State the preparation type.
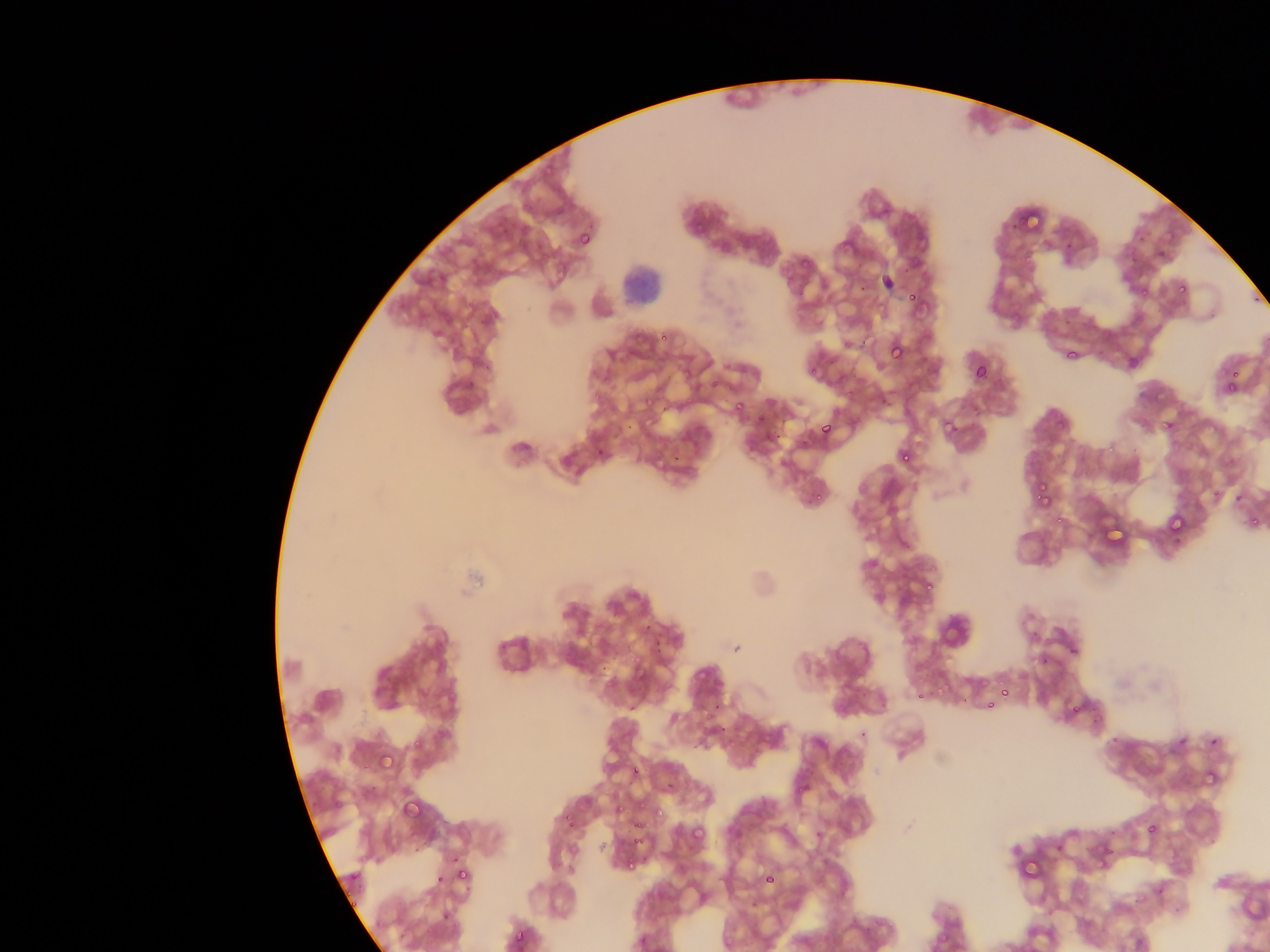
This is a thin smear.

plasmodium_parasite_locations: 'approximate bounding boxes as (left, top, right, bottom) in pixels: (1025, 211, 1044, 231), (689, 221, 705, 235), (578, 231, 593, 247), (798, 259, 809, 269), (1177, 284, 1187, 295), (1136, 288, 1149, 303), (907, 290, 921, 305), (660, 332, 670, 342), (887, 340, 904, 360), (1065, 349, 1077, 359), (808, 354, 820, 374), (972, 364, 987, 380), (1228, 369, 1239, 380), (1223, 374, 1238, 392), (844, 381, 857, 399), (583, 388, 606, 403), (637, 396, 654, 413), (734, 401, 746, 414), (756, 415, 766, 425), (1163, 419, 1175, 432), (941, 421, 955, 432), (820, 422, 834, 435), (1103, 444, 1117, 457), (898, 449, 913, 463), (671, 453, 680, 461), (1034, 480, 1048, 496), (1207, 489, 1220, 503), (807, 490, 824, 503), (1039, 494, 1053, 508), (1169, 514, 1187, 534), (1055, 515, 1065, 525), (1249, 515, 1260, 532), (1105, 518, 1125, 543), (922, 578, 937, 593), (639, 618, 654, 633), (652, 639, 668, 653), (1069, 646, 1079, 656), (936, 680, 949, 700), (1001, 690, 1010, 698), (916, 691, 925, 700), (985, 700, 995, 709), (1068, 705, 1080, 716), (703, 714, 711, 725), (712, 723, 728, 737), (1109, 734, 1120, 744), (411, 736, 424, 751), (1208, 737, 1219, 746), (377, 751, 393, 768), (631, 766, 641, 777), (1194, 774, 1226, 789), (401, 798, 421, 817), (637, 798, 648, 809), (612, 799, 627, 816), (649, 806, 662, 819), (559, 812, 574, 826), (563, 817, 574, 829), (634, 819, 644, 832), (1146, 822, 1158, 834), (690, 825, 704, 840), (631, 835, 644, 847), (1021, 850, 1045, 881), (1085, 853, 1117, 871), (625, 856, 641, 876), (455, 867, 470, 885), (435, 871, 447, 884), (762, 872, 776, 885), (441, 910, 451, 921), (513, 928, 528, 946)'
image_size: 1270×952 pixels
capture: mobile-phone photograph through a microscope
field_of_view: single
leukocyte_locations: 'approximate bounding boxes as (left, top, right, bottom) in pixels: (617, 255, 662, 313)'
country: Ghana